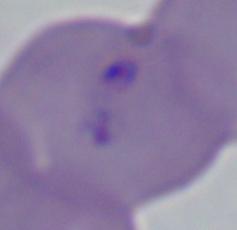
Summary:
  - Identification: Babesia
  - Magnification: 1000x
  - Modality: photomicrograph